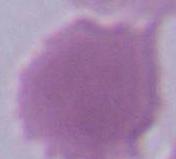

An erythrocyte is shown. Captured at 1000x magnification. Micrograph.